Identify the blood parasite species.
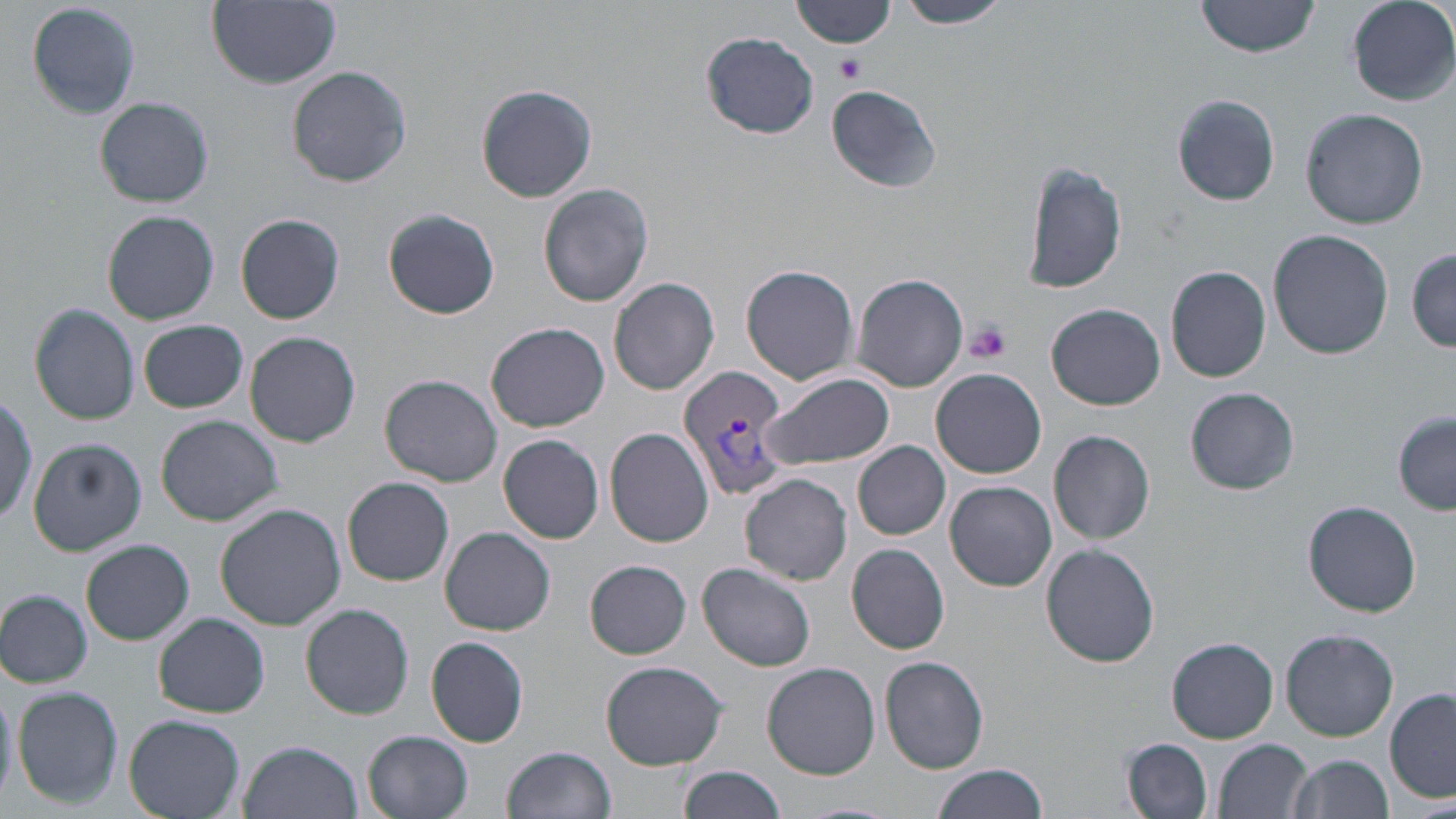
Plasmodium vivax.

Approximate bounding boxes as (x1, y1, x2, y2) in pixels. Uninfected red blood cell locations: (26, 0, 144, 120), (207, 0, 341, 88), (793, 0, 901, 50), (896, 0, 1011, 29), (1197, 0, 1319, 58), (1348, 0, 1455, 104), (699, 32, 819, 139), (288, 66, 412, 189), (476, 83, 598, 204), (826, 83, 944, 193), (1172, 94, 1280, 207), (94, 96, 215, 207), (1302, 107, 1428, 229), (1022, 162, 1127, 295), (537, 184, 654, 306), (383, 208, 500, 319), (102, 209, 219, 324), (236, 213, 346, 325), (1268, 230, 1395, 360), (1409, 247, 1456, 352), (742, 263, 859, 386), (1166, 265, 1272, 383), (849, 272, 968, 392), (609, 277, 719, 397), (1046, 302, 1166, 411), (29, 303, 141, 425), (137, 318, 249, 413), (486, 321, 610, 432), (245, 331, 361, 447), (931, 368, 1047, 478), (759, 372, 895, 472), (381, 375, 503, 487), (1185, 387, 1299, 495), (0, 392, 40, 525), (1393, 413, 1455, 515), (156, 415, 283, 527), (605, 427, 715, 548), (1049, 430, 1155, 545), (497, 434, 606, 545), (25, 436, 146, 554), (854, 441, 951, 539), (718, 471, 842, 667), (740, 473, 852, 585), (343, 476, 455, 585), (946, 481, 1056, 591), (1304, 500, 1422, 617), (215, 503, 346, 630), (440, 526, 556, 635), (80, 539, 195, 646), (1042, 543, 1160, 668), (847, 544, 951, 654), (585, 561, 691, 658), (698, 561, 817, 672), (1, 587, 95, 687), (300, 603, 414, 719), (153, 612, 270, 717), (1281, 629, 1397, 740), (426, 636, 530, 746), (1168, 637, 1278, 743), (881, 656, 988, 773), (600, 659, 727, 770), (762, 662, 881, 779), (11, 687, 124, 809), (1385, 688, 1456, 804), (124, 714, 245, 819), (363, 730, 473, 818), (1123, 738, 1213, 819), (1214, 738, 1313, 819), (239, 740, 363, 819), (501, 746, 616, 819), (1287, 753, 1393, 819), (931, 762, 1052, 819), (680, 765, 789, 819), (795, 801, 901, 819). Plasmodium vivax-infected red blood cell locations: (681, 364, 795, 505). Platelet locations: (834, 52, 867, 83), (965, 322, 1010, 363). May-Grünwald-Giemsa stain. Single field of view. Thin blood film. Captured at 1000x magnification. Light microscopy. Image is 1456×819 pixels.